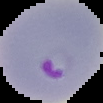
malaria status = parasitized
image size = 103×103 pixels
preparation = thin blood smear
image type = cell region segmented out of the field of view; surrounding area masked to black